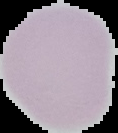
{
  "image_type": "segmented cell region with the area outside set to black",
  "malaria_status": "uninfected",
  "preparation": "thin blood smear",
  "image_size": "118×133 pixels"
}